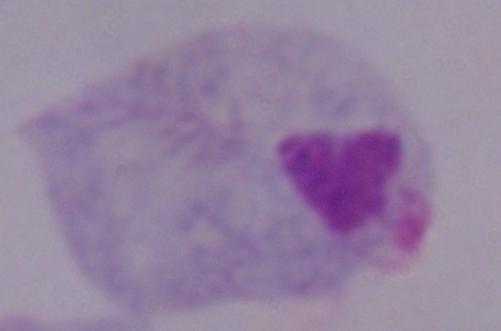
Micrograph. Captured at 1000x magnification. A trichomonad is shown.